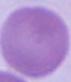
identification = red blood cell
magnification = 1000x
modality = micrograph